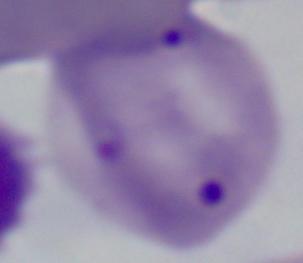

magnification = 1000x
modality = photomicrograph
identification = Babesia